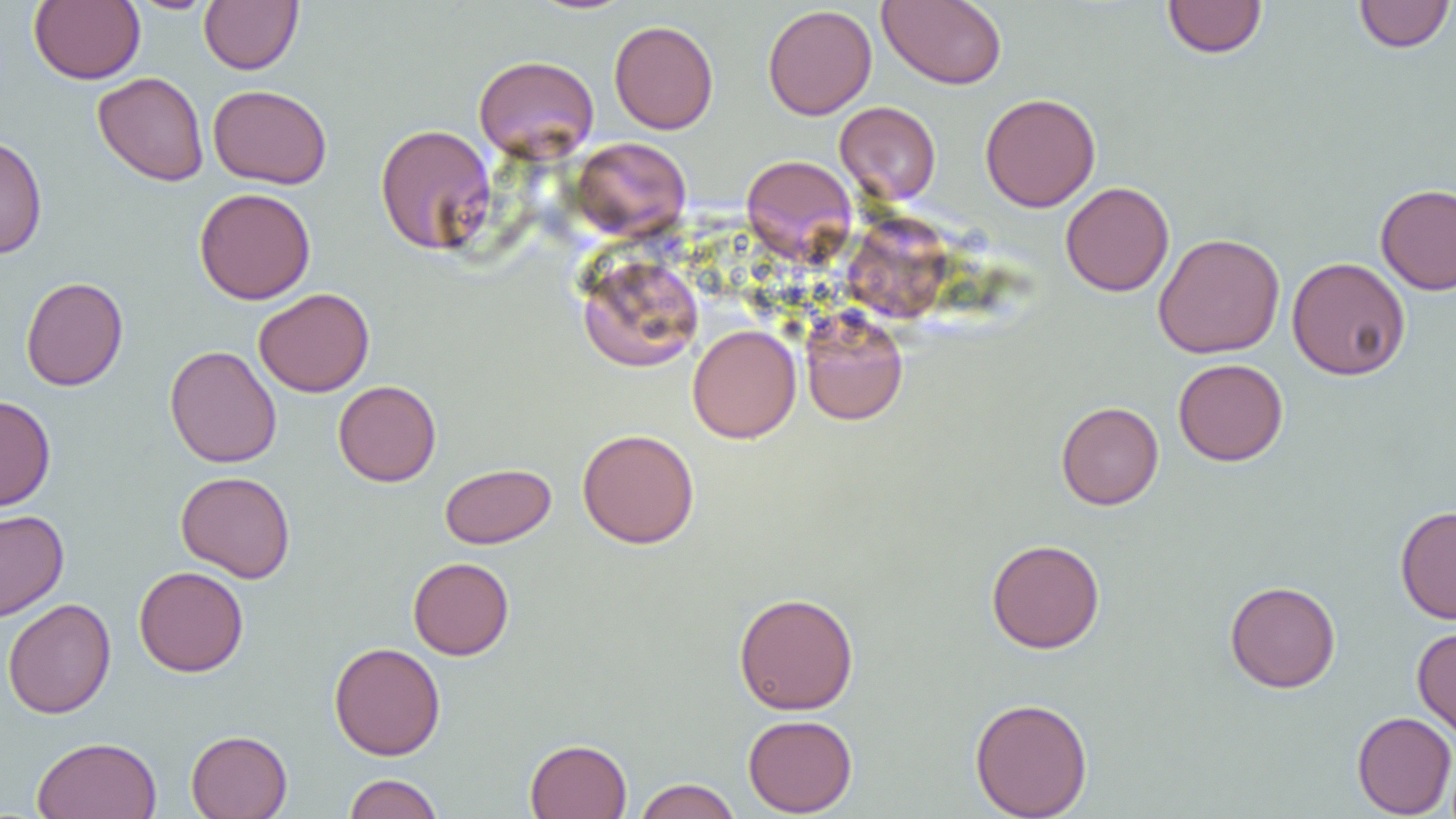

slide-level diagnosis = no evidence of blood parasites
magnification = 1000x
modality = optical microscopy
image size = 1456×819 pixels
uninfected red blood cell locations = approximate bounding boxes as named x1/y1/x2/y2 corners in pixels: (x1=29, y1=0, x2=145, y2=84), (x1=127, y1=0, x2=219, y2=14), (x1=200, y1=0, x2=303, y2=74), (x1=527, y1=0, x2=637, y2=15), (x1=877, y1=0, x2=1007, y2=90), (x1=1162, y1=0, x2=1267, y2=59), (x1=1353, y1=1, x2=1455, y2=52), (x1=763, y1=4, x2=877, y2=120), (x1=609, y1=20, x2=719, y2=134), (x1=473, y1=54, x2=599, y2=162), (x1=92, y1=71, x2=209, y2=186), (x1=208, y1=84, x2=332, y2=189), (x1=980, y1=92, x2=1101, y2=212), (x1=835, y1=101, x2=941, y2=205), (x1=375, y1=123, x2=496, y2=255), (x1=0, y1=134, x2=47, y2=260), (x1=571, y1=136, x2=692, y2=240), (x1=741, y1=154, x2=856, y2=262), (x1=1060, y1=181, x2=1175, y2=297), (x1=1376, y1=184, x2=1456, y2=295), (x1=194, y1=187, x2=316, y2=304), (x1=847, y1=212, x2=952, y2=328), (x1=1153, y1=232, x2=1285, y2=359), (x1=577, y1=255, x2=704, y2=372), (x1=1287, y1=257, x2=1411, y2=381), (x1=20, y1=276, x2=128, y2=391), (x1=253, y1=288, x2=375, y2=397), (x1=800, y1=311, x2=909, y2=426), (x1=687, y1=324, x2=801, y2=443), (x1=164, y1=345, x2=282, y2=468), (x1=1173, y1=358, x2=1288, y2=466), (x1=333, y1=380, x2=441, y2=487), (x1=0, y1=395, x2=56, y2=512), (x1=1056, y1=401, x2=1164, y2=510), (x1=577, y1=428, x2=700, y2=549), (x1=440, y1=463, x2=555, y2=549), (x1=175, y1=470, x2=296, y2=583), (x1=1395, y1=505, x2=1456, y2=624), (x1=0, y1=510, x2=69, y2=622), (x1=986, y1=539, x2=1105, y2=654), (x1=408, y1=557, x2=514, y2=660), (x1=134, y1=565, x2=249, y2=677), (x1=1225, y1=580, x2=1340, y2=693), (x1=733, y1=592, x2=859, y2=715), (x1=2, y1=598, x2=116, y2=718), (x1=1412, y1=626, x2=1456, y2=741), (x1=329, y1=642, x2=445, y2=760), (x1=969, y1=697, x2=1093, y2=818), (x1=1352, y1=711, x2=1456, y2=818), (x1=743, y1=714, x2=858, y2=817), (x1=186, y1=730, x2=292, y2=819), (x1=31, y1=736, x2=162, y2=819), (x1=524, y1=739, x2=632, y2=819), (x1=344, y1=773, x2=444, y2=819), (x1=634, y1=778, x2=741, y2=819)
field of view = single
preparation = thin blood film